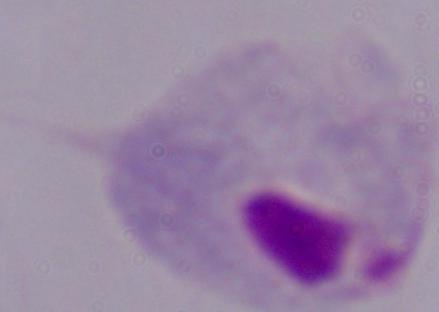

modality = micrograph
identification = trichomonad
magnification = 1000x